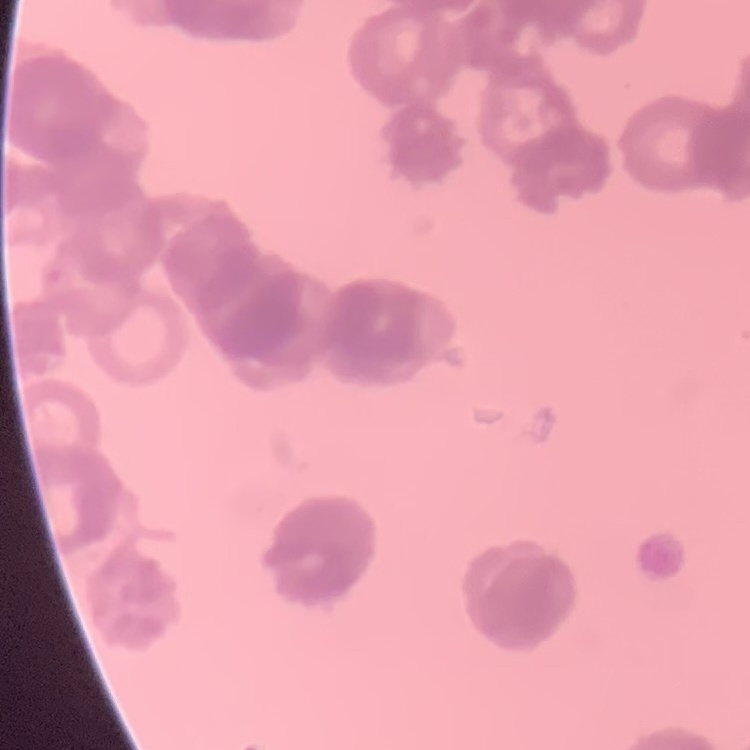
The red blood cells exhibit rouleaux formation. Square crop of a larger photomicrograph. Field's or Giemsa stain. Thin blood film.